Assess the morphology of the red blood cells.
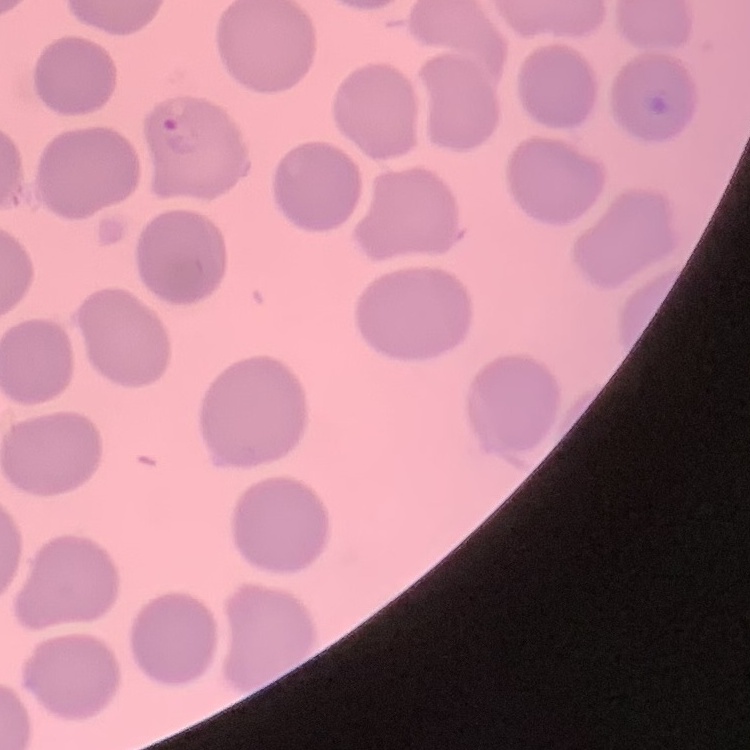
No rouleaux formation.

One tile cut from a larger photomicrograph. Stained with either Field's or Giemsa. Thin peripheral smear.